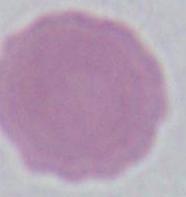

magnification = 1000x
modality = photomicrograph
identification = red blood cell